Point out each leukocyte.
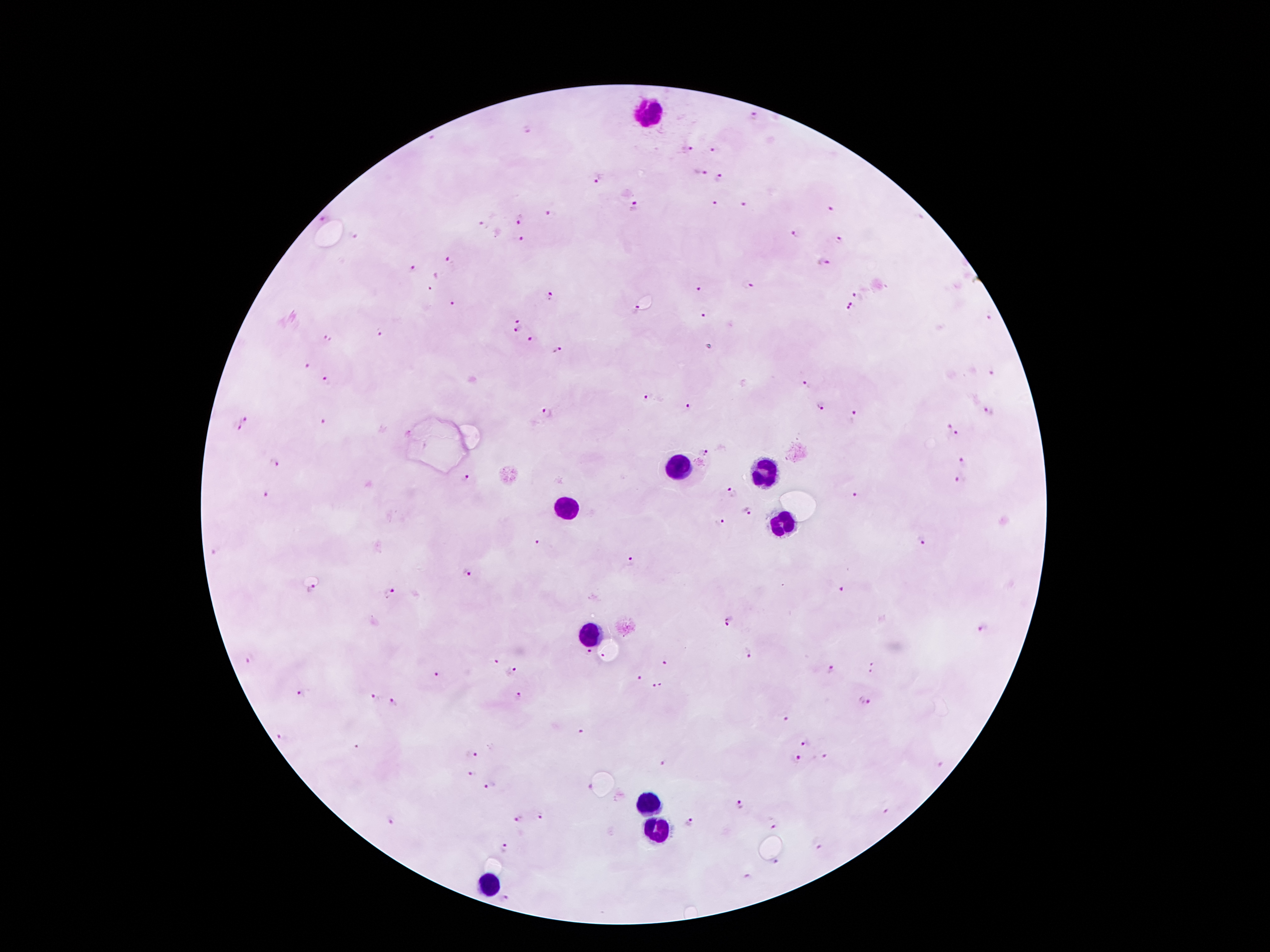

Approximate centers as (x, y) in pixels.
Leukocytes: (648, 113), (676, 466), (760, 473), (567, 509), (785, 529), (586, 630), (645, 799), (656, 830), (488, 885).

Summary:
  - Malaria parasite locations: (755, 118), (525, 129), (433, 137), (688, 151), (713, 151), (702, 172), (719, 177), (599, 180), (713, 202), (743, 204), (635, 205), (831, 208), (553, 212), (320, 218), (519, 218), (483, 225), (797, 233), (353, 236), (521, 239), (839, 240), (450, 258), (823, 262), (412, 269), (747, 285), (431, 288), (699, 289), (551, 294), (857, 294), (454, 305), (853, 305), (638, 310), (849, 310), (703, 316), (989, 318), (518, 322), (515, 332), (380, 333), (529, 338), (328, 340), (556, 351), (305, 365), (992, 372), (326, 381), (807, 385), (646, 397), (688, 407), (819, 407), (549, 412), (987, 412), (853, 416), (245, 419), (322, 424), (236, 425), (949, 426), (958, 433), (705, 452), (276, 462), (964, 462), (466, 480), (960, 480), (267, 493), (732, 493), (854, 496), (749, 510), (720, 522), (922, 540), (538, 544), (215, 552), (629, 562), (468, 573), (311, 588), (843, 590), (390, 593), (730, 622), (982, 628), (588, 651), (750, 653), (602, 655), (495, 660), (251, 661), (665, 663), (873, 668), (830, 670), (513, 671), (437, 675), (638, 678), (659, 686), (302, 693), (374, 696), (519, 697), (866, 700), (395, 702), (786, 720), (581, 730), (282, 736), (807, 743), (356, 748), (471, 754), (825, 757), (796, 758), (664, 763), (472, 774), (491, 785), (741, 805), (886, 813), (543, 818), (519, 819), (392, 820), (689, 824), (773, 825), (819, 845), (504, 849), (777, 863), (749, 877), (506, 897)
  - Preparation: thick blood smear
  - Image size: 1270×952 pixels
  - Capture: smartphone camera through the microscope eyepiece
  - Patient malaria status: positive for Plasmodium falciparum
  - Stain: Giemsa
  - Field of view: one from this slide
  - Magnification: 100x